State which parasite is depicted.
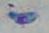
This is Toxoplasma gondii.

Summary:
  - Magnification: 1000x
  - Modality: photomicrograph